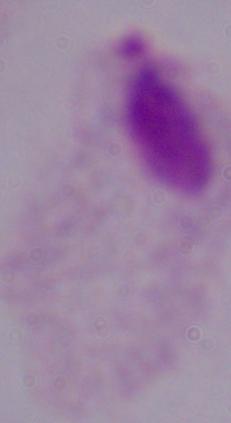
Summary:
  - Identification: trichomonad
  - Magnification: 1000x
  - Modality: photomicrograph